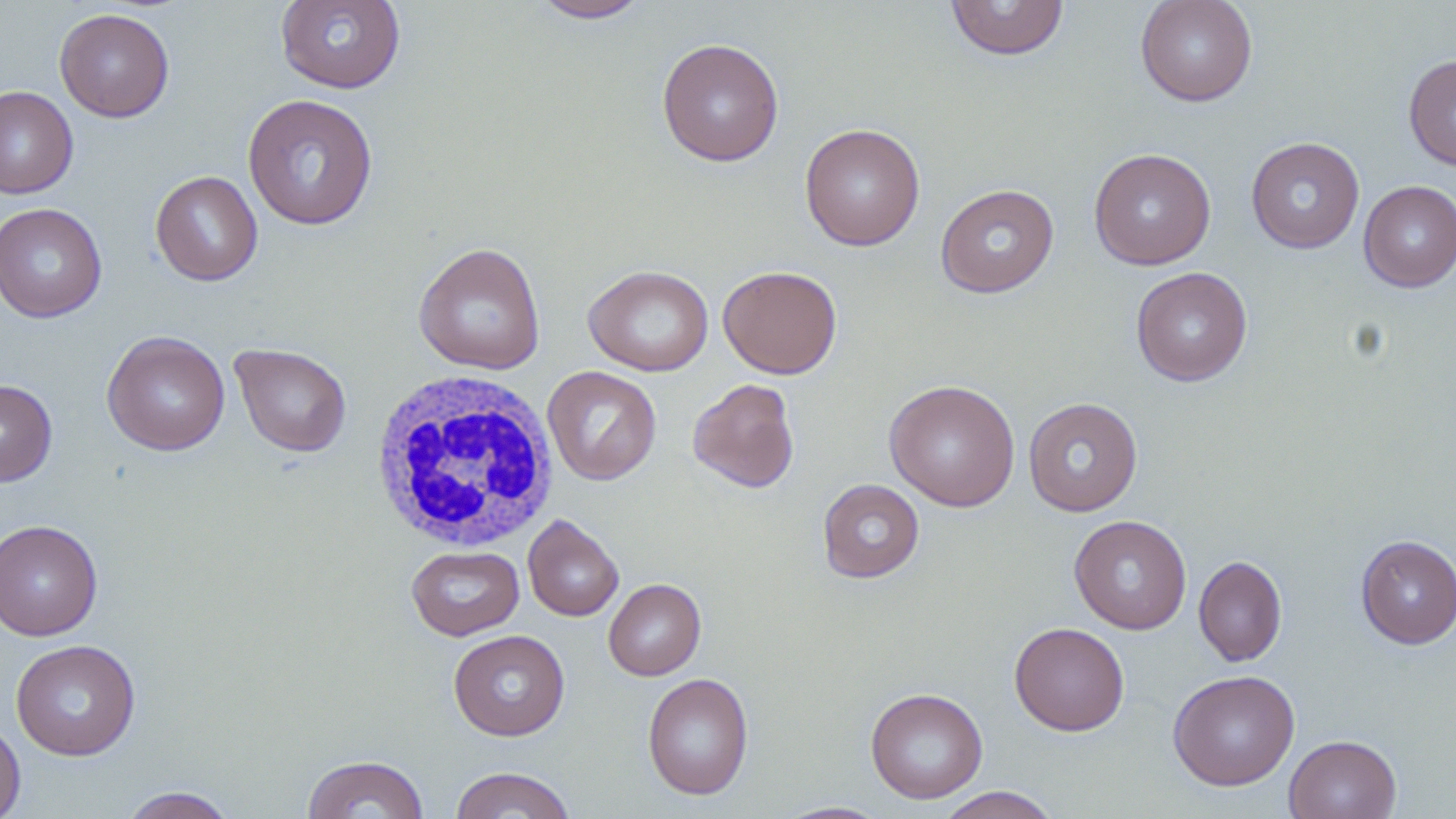

Approximate bounding boxes as (x1, y1, x2, y2) in pixels. Uninfected red blood cell locations: (275, 0, 406, 94), (944, 0, 1071, 61), (1135, 0, 1258, 107), (530, 1, 652, 23), (54, 8, 175, 122), (656, 38, 784, 166), (1403, 53, 1456, 171), (0, 85, 78, 198), (242, 93, 379, 231), (800, 123, 925, 251), (1246, 137, 1364, 254), (1089, 148, 1216, 270), (150, 170, 263, 286), (1358, 180, 1456, 292), (935, 183, 1059, 298), (0, 203, 107, 323), (413, 242, 546, 375), (583, 264, 714, 377), (718, 265, 842, 379), (1130, 267, 1252, 387), (101, 330, 231, 456), (230, 342, 352, 457), (543, 366, 662, 486), (0, 378, 58, 486), (687, 378, 800, 493), (883, 378, 1021, 512), (1023, 397, 1143, 516), (817, 478, 925, 583), (523, 515, 623, 621), (1069, 515, 1192, 634), (1, 518, 103, 642), (1355, 535, 1456, 649), (406, 545, 524, 640), (1193, 555, 1288, 666), (603, 578, 706, 680), (1009, 622, 1130, 736), (449, 629, 570, 740), (11, 639, 141, 761), (1167, 670, 1301, 790), (642, 672, 754, 801), (865, 686, 988, 804), (0, 718, 26, 819), (1283, 734, 1402, 819), (302, 754, 429, 818), (449, 766, 577, 818), (934, 786, 1062, 818), (118, 787, 238, 819), (774, 801, 891, 818). White blood cell locations: (368, 368, 560, 553). Slide-level diagnosis: negative for blood parasites. Light microscopy. Thin blood film. Image is 1456×819 pixels. 1000x magnification. May-Grünwald-Giemsa-stained preparation. Single field of view.